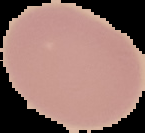
malaria status = uninfected
preparation = thin blood film
image size = 145×133 pixels
image type = cell region segmented out of the field of view; surrounding area masked to black